Give the position of every Plasmodium parasite.
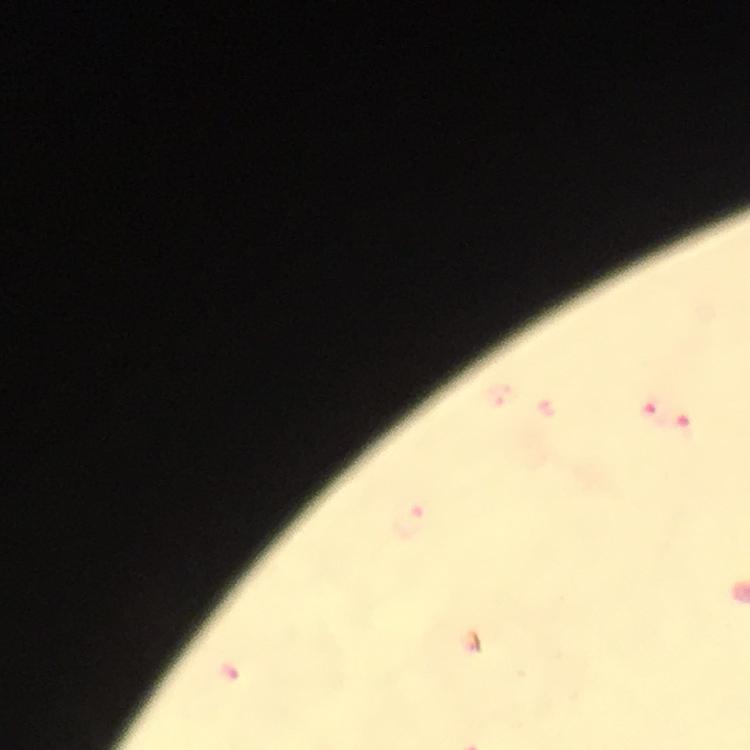

Approximate centers as [x, y] in pixels.
Plasmodium parasites: [652, 409], [685, 424], [412, 520].

image size = 750×750 pixels
stain = Giemsa
immersion oil = used
capture = smartphone photograph through a microscope
magnification = 100x
context = from a malaria diagnostic workup
cropped from = a single field of view
preparation = thick smear